Comment on the morphology of the erythrocytes.
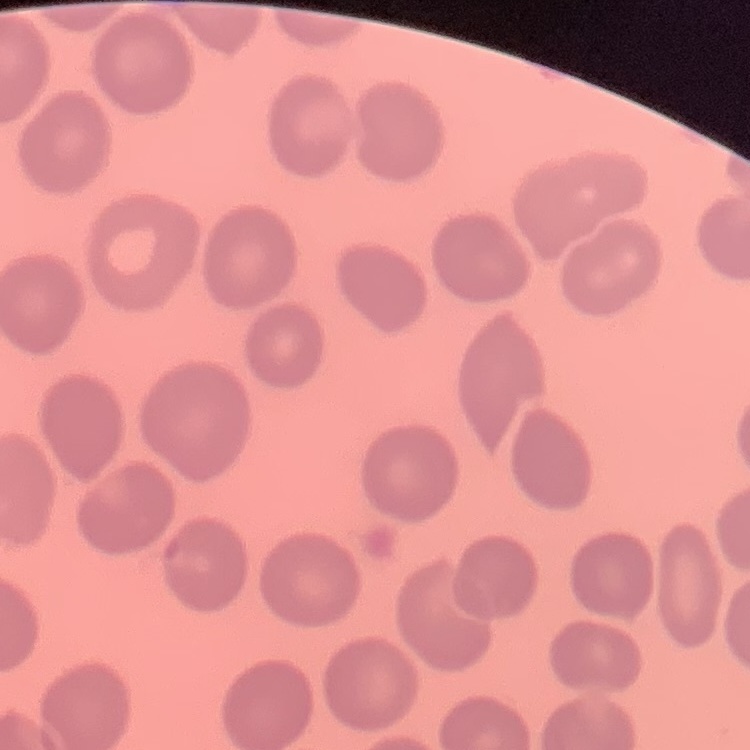

They show no rouleaux formation.

preparation = thin blood smear
stain = Field's or Giemsa
image type = square crop of a larger photomicrograph